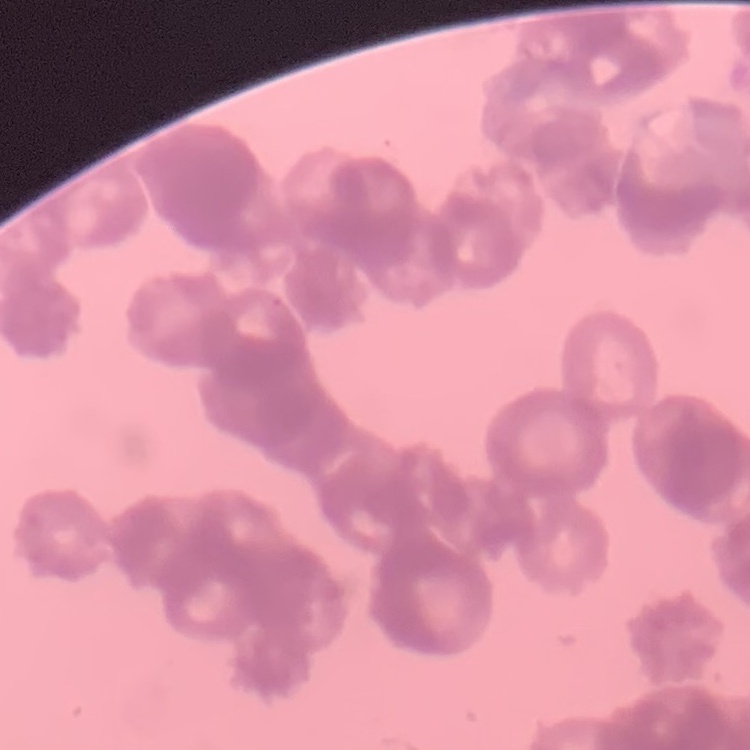

Summary:
  - Red blood cell morphology: rouleaux formation
  - Stain: Field's or Giemsa
  - Image type: one tile cut from a larger photomicrograph
  - Preparation: thin peripheral smear